Locate platelets.
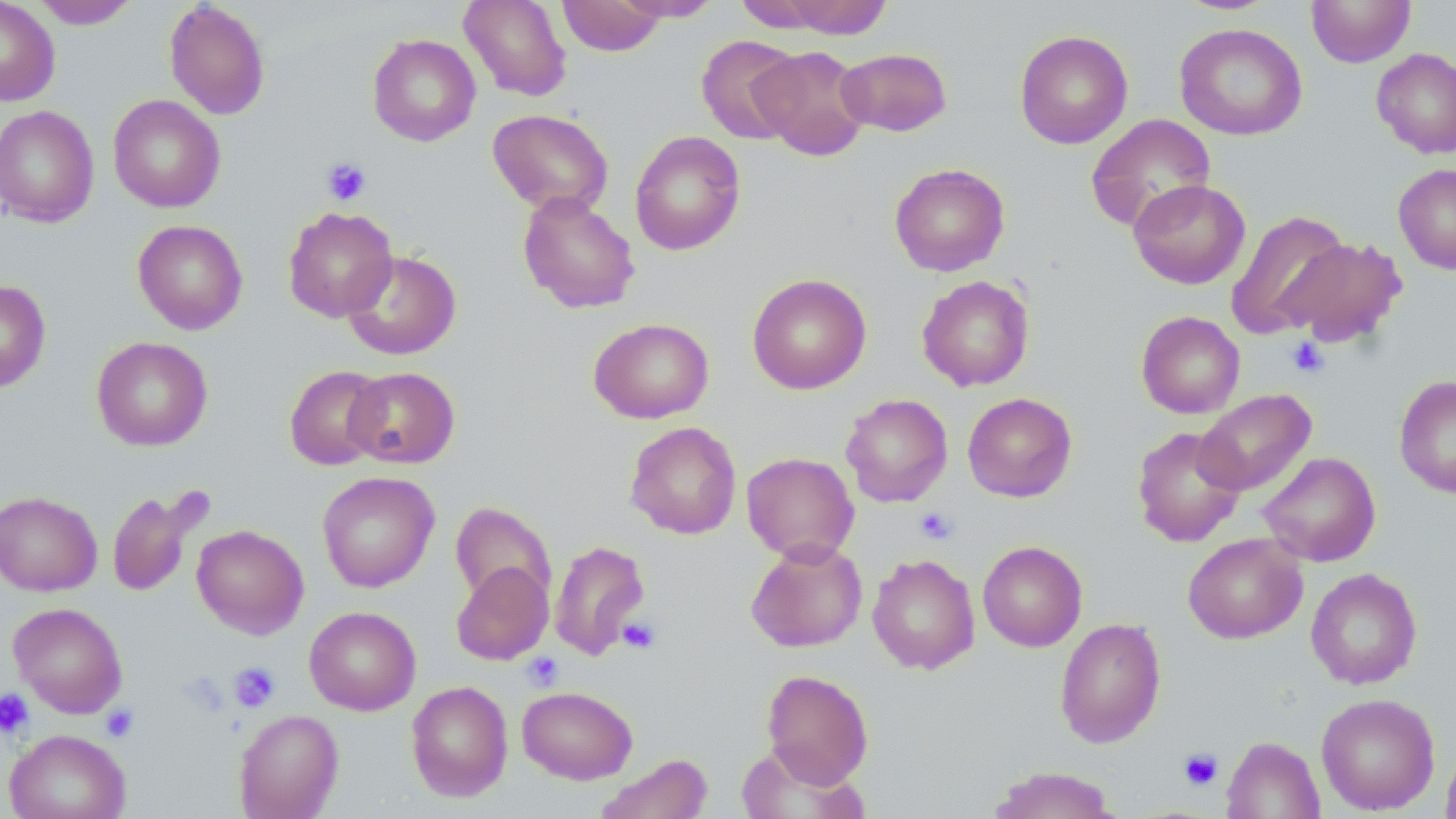

Approximate bounding boxes as named x1/y1/x2/y2 corners in pixels.
Platelets: (x1=321, y1=157, x2=371, y2=206), (x1=1286, y1=337, x2=1330, y2=378), (x1=914, y1=507, x2=958, y2=545), (x1=618, y1=617, x2=661, y2=655), (x1=522, y1=652, x2=564, y2=691), (x1=228, y1=662, x2=280, y2=711), (x1=0, y1=688, x2=35, y2=740), (x1=100, y1=704, x2=140, y2=742), (x1=1178, y1=748, x2=1224, y2=790).

Uninfected red blood cell locations: (x1=0, y1=0, x2=60, y2=106), (x1=458, y1=0, x2=572, y2=102), (x1=556, y1=0, x2=667, y2=56), (x1=612, y1=0, x2=723, y2=22), (x1=734, y1=0, x2=836, y2=31), (x1=778, y1=0, x2=892, y2=39), (x1=1306, y1=0, x2=1416, y2=67), (x1=32, y1=1, x2=141, y2=29), (x1=164, y1=1, x2=271, y2=120), (x1=1174, y1=23, x2=1307, y2=141), (x1=1014, y1=29, x2=1133, y2=149), (x1=367, y1=34, x2=481, y2=146), (x1=696, y1=35, x2=804, y2=144), (x1=751, y1=45, x2=871, y2=160), (x1=836, y1=47, x2=952, y2=137), (x1=1371, y1=47, x2=1456, y2=159), (x1=108, y1=94, x2=226, y2=213), (x1=0, y1=105, x2=99, y2=227), (x1=487, y1=108, x2=613, y2=215), (x1=1085, y1=114, x2=1216, y2=233), (x1=629, y1=130, x2=746, y2=256), (x1=889, y1=163, x2=1010, y2=276), (x1=1393, y1=163, x2=1456, y2=274), (x1=1128, y1=179, x2=1250, y2=289), (x1=517, y1=191, x2=639, y2=314), (x1=282, y1=206, x2=398, y2=322), (x1=1226, y1=210, x2=1352, y2=339), (x1=132, y1=219, x2=248, y2=335), (x1=1281, y1=237, x2=1408, y2=347), (x1=342, y1=250, x2=461, y2=360), (x1=747, y1=273, x2=872, y2=395), (x1=917, y1=275, x2=1034, y2=391), (x1=0, y1=280, x2=51, y2=393), (x1=1136, y1=311, x2=1245, y2=418), (x1=588, y1=317, x2=714, y2=423), (x1=91, y1=336, x2=212, y2=451), (x1=284, y1=365, x2=389, y2=471), (x1=344, y1=366, x2=460, y2=468), (x1=1394, y1=375, x2=1456, y2=498), (x1=1194, y1=389, x2=1316, y2=496), (x1=962, y1=392, x2=1077, y2=502), (x1=840, y1=393, x2=953, y2=507), (x1=624, y1=421, x2=742, y2=540), (x1=1132, y1=425, x2=1246, y2=547), (x1=1258, y1=451, x2=1381, y2=567), (x1=741, y1=452, x2=859, y2=563), (x1=316, y1=471, x2=440, y2=593), (x1=107, y1=489, x2=198, y2=597), (x1=0, y1=491, x2=102, y2=596), (x1=450, y1=501, x2=557, y2=609), (x1=192, y1=524, x2=309, y2=639), (x1=1183, y1=532, x2=1307, y2=644), (x1=549, y1=539, x2=650, y2=660), (x1=745, y1=539, x2=867, y2=653), (x1=978, y1=540, x2=1087, y2=652), (x1=867, y1=554, x2=980, y2=674), (x1=451, y1=561, x2=553, y2=665), (x1=1306, y1=567, x2=1422, y2=689), (x1=8, y1=602, x2=127, y2=718), (x1=304, y1=606, x2=421, y2=715), (x1=1054, y1=617, x2=1166, y2=748), (x1=761, y1=669, x2=874, y2=789), (x1=406, y1=680, x2=513, y2=802), (x1=517, y1=685, x2=638, y2=784), (x1=1316, y1=693, x2=1440, y2=815), (x1=233, y1=708, x2=344, y2=819), (x1=4, y1=729, x2=130, y2=819), (x1=1221, y1=735, x2=1325, y2=819), (x1=1441, y1=741, x2=1456, y2=819), (x1=735, y1=742, x2=864, y2=819), (x1=594, y1=753, x2=712, y2=819), (x1=987, y1=765, x2=1121, y2=819). Slide-level diagnosis: negative for blood parasites. May-Grünwald-Giemsa stain. Thin blood smear. Captured at 1000x magnification. Image is 1456×819 pixels. Single field of view. Light microscopy.